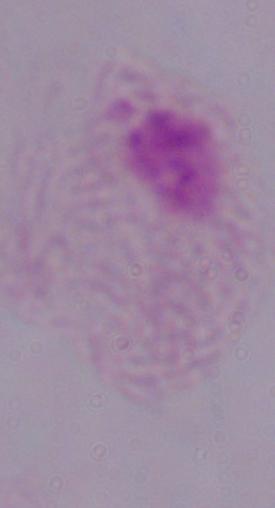
Summary:
  - Identification: trichomonad
  - Magnification: 1000x
  - Modality: micrograph